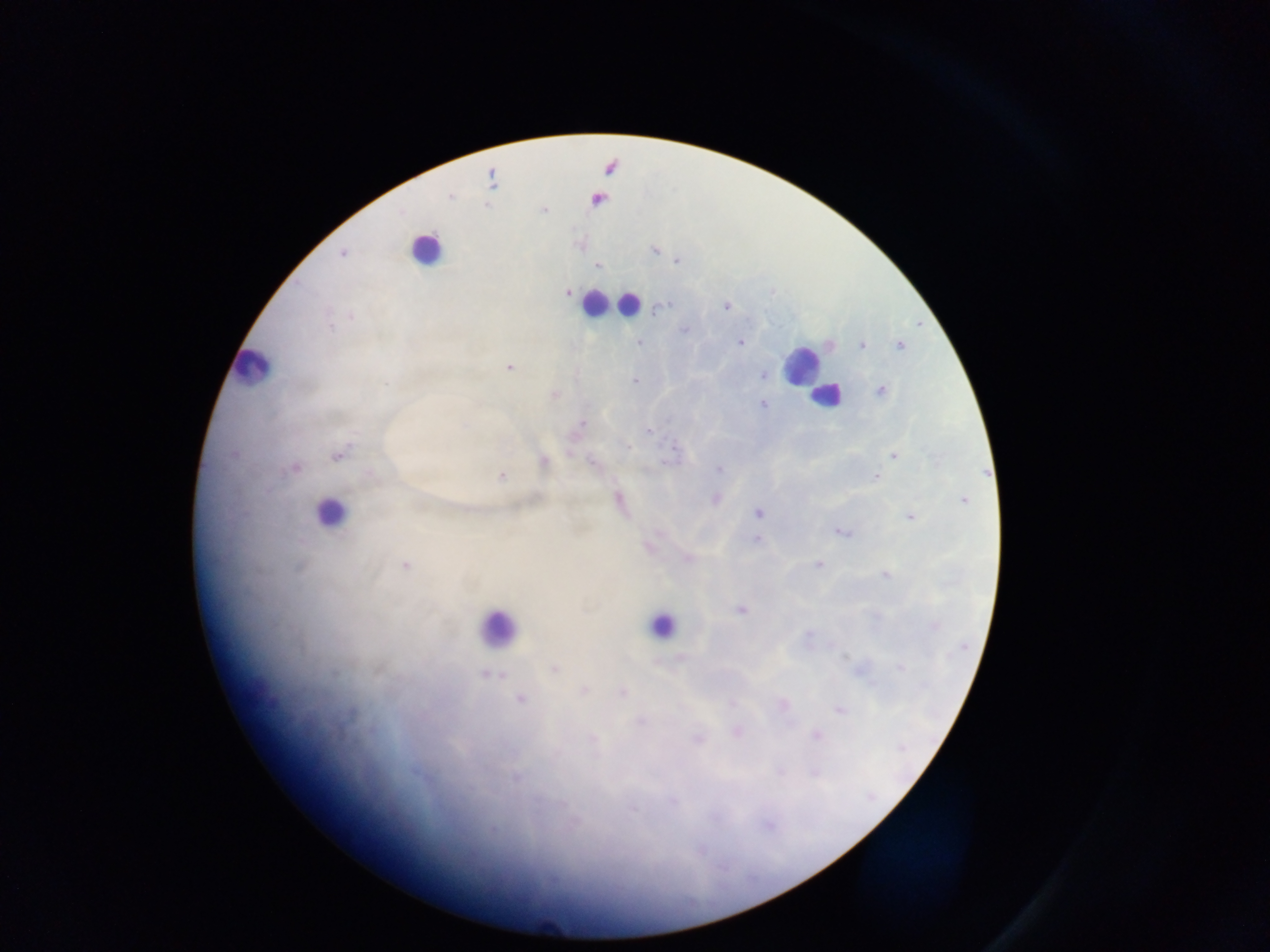

Approximate centers as {x, y} in pixels.
Summary:
  - Plasmodium parasite locations: {450, 196}, {544, 210}, {654, 250}, {342, 254}, {677, 261}, {598, 266}, {567, 293}, {726, 305}, {664, 307}, {352, 317}, {330, 327}, {685, 331}, {639, 342}, {740, 342}, {900, 345}, {861, 346}, {509, 367}, {763, 375}, {634, 381}, {386, 383}, {881, 391}, {553, 395}, {762, 404}, {581, 424}, {649, 431}, {628, 446}, {674, 451}, {233, 454}, {337, 455}, {894, 456}, {543, 460}, {592, 462}, {295, 469}, {719, 469}, {501, 476}, {876, 477}, {715, 499}, {963, 500}, {618, 501}, {757, 513}, {910, 517}, {840, 532}, {756, 539}, {650, 546}, {688, 558}, {818, 564}, {405, 565}, {885, 575}, {740, 610}, {935, 627}, {808, 635}, {845, 657}, {900, 667}, {554, 668}, {486, 675}, {584, 690}, {622, 692}, {521, 699}, {732, 703}, {782, 704}, {838, 709}, {640, 721}, {736, 731}, {817, 735}, {593, 739}, {697, 739}, {902, 748}, {779, 772}, {814, 772}, {515, 778}, {672, 802}, {632, 809}, {768, 825}
  - Leukocyte locations: {426, 248}, {594, 303}, {629, 304}, {801, 364}, {252, 365}, {824, 397}, {330, 512}, {663, 624}, {496, 627}
  - Preparation: thick blood smear
  - Image size: 1270×952 pixels
  - Capture: mobile-phone photograph through a microscope
  - Field of view: single
  - Country: Ghana